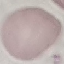
Summary:
  - Result: no malaria parasites seen
  - Capture: smartphone through the microscope eyepiece
  - Stain: Giemsa
  - Preparation: thin blood smear
  - Image type: cell patch, automatically extracted from a larger field of view and resized to 64 × 64 pixels